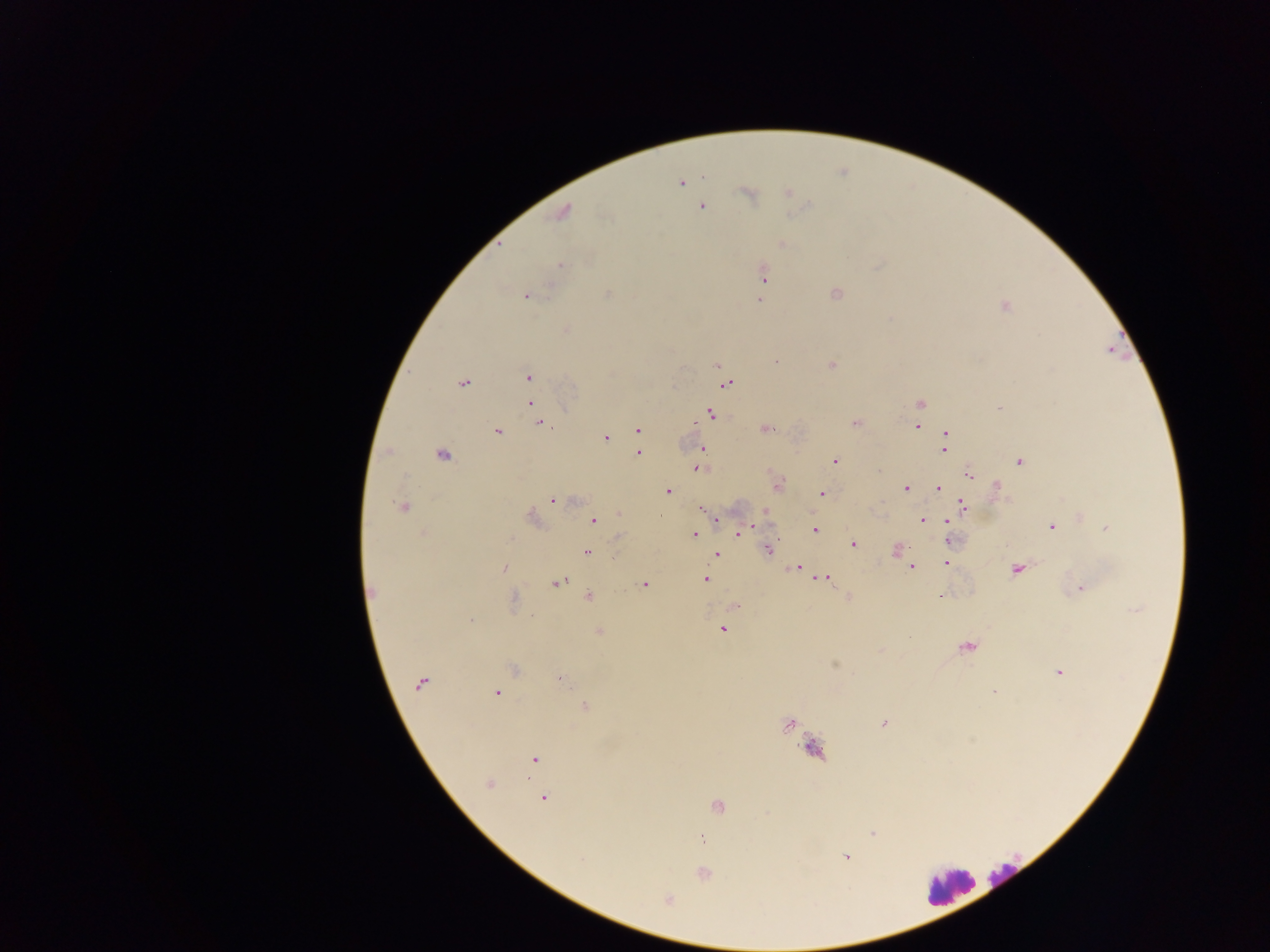

Approximate centers as [x, y] in pixels.
Summary:
  - Malaria parasite locations: [704, 176], [680, 183], [788, 192], [748, 194], [702, 207], [562, 212], [782, 244], [560, 265], [763, 274], [607, 293], [836, 294], [526, 296], [759, 300], [1005, 306], [775, 362], [716, 365], [831, 366], [528, 377], [463, 383], [725, 384], [530, 403], [920, 404], [999, 408], [711, 414], [855, 422], [540, 423], [916, 427], [766, 429], [637, 430], [497, 432], [947, 433], [605, 437], [944, 448], [701, 449], [638, 453], [443, 455], [834, 461], [1019, 462], [698, 468], [878, 470], [969, 474], [996, 486], [906, 488], [939, 488], [668, 492], [822, 494], [553, 500], [962, 506], [403, 508], [702, 509], [765, 513], [619, 514], [533, 518], [594, 520], [716, 520], [923, 520], [948, 520], [1051, 527], [1106, 528], [744, 529], [815, 529], [423, 533], [694, 533], [739, 533], [618, 537], [949, 541], [853, 544], [768, 548], [896, 550], [587, 552], [716, 555], [946, 563], [504, 568], [796, 568], [911, 568], [1017, 570], [826, 577], [705, 579], [559, 582], [644, 584], [1080, 589], [373, 592], [590, 596], [939, 596], [513, 599], [735, 606], [470, 620], [722, 629], [599, 632], [967, 647], [834, 665], [513, 669], [1059, 673], [562, 679], [420, 683], [994, 691], [497, 693], [585, 707], [883, 722], [789, 725], [814, 748], [534, 759], [490, 784], [544, 798], [718, 807], [872, 834], [702, 838], [846, 857], [582, 859], [704, 873], [668, 899]
  - Leukocyte locations: [1004, 876], [949, 886]
  - Preparation: thick blood smear
  - Country: Ghana
  - Capture: mobile-phone photograph through a microscope
  - Field of view: single
  - Image size: 1270×952 pixels